Point out each malaria parasite.
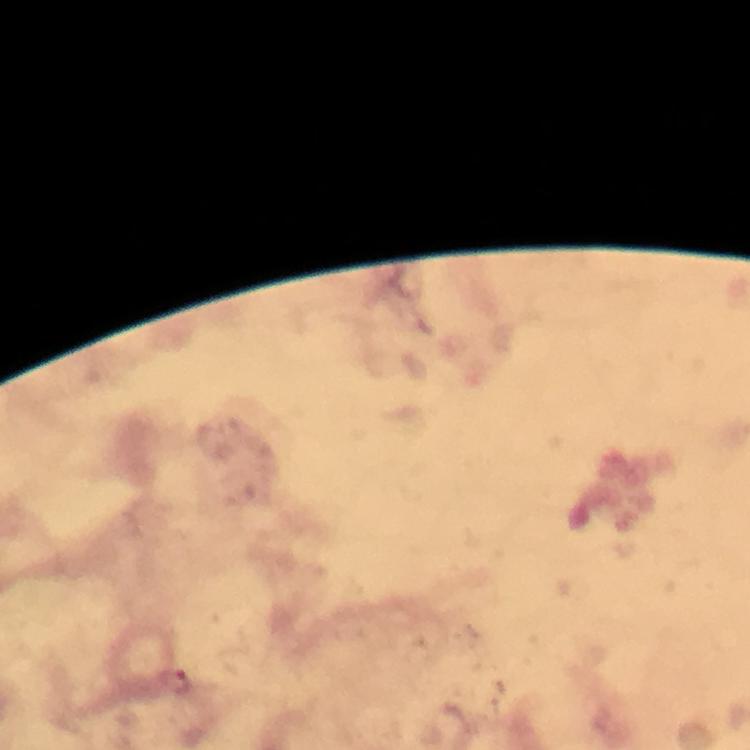

Approximate centers as [x, y] in pixels.
Malaria parasites: [179, 681].

{
  "preparation": "thick blood film",
  "capture": "smartphone photograph through a microscope",
  "magnification": "100x",
  "context": "from a diagnostic examination for malaria",
  "stain": "Giemsa",
  "cropped_from": "one field of view",
  "image_size": "750×750 pixels",
  "immersion_oil": "used"
}